Assess the morphology of the red blood cells.
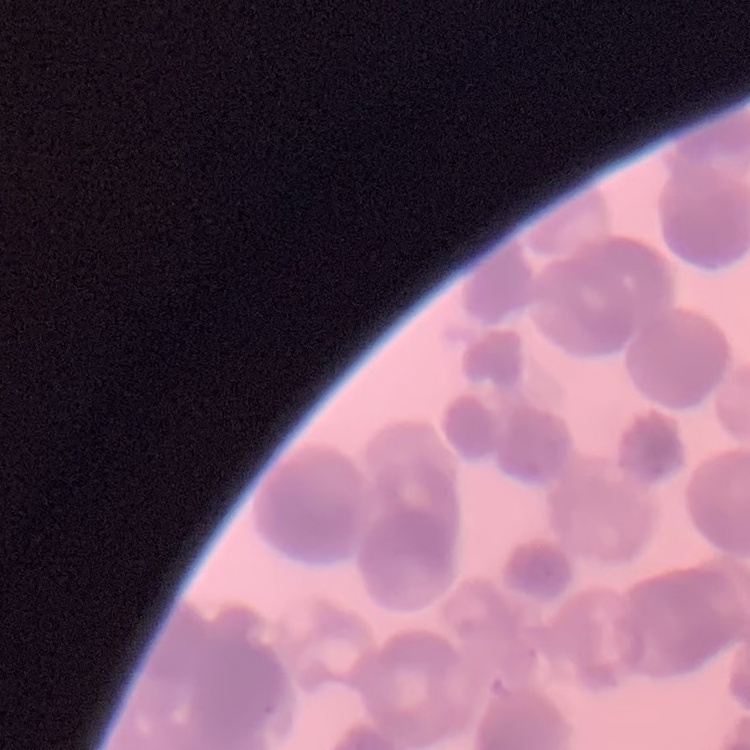

They show rouleaux formation.

Summary:
  - Stain: Field's or Giemsa
  - Preparation: thin blood smear
  - Image type: square crop of a larger photomicrograph